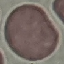
Summary:
  - Malaria status: uninfected
  - Stain: Giemsa
  - Image type: cell patch, automatically extracted from a larger field of view and resized to 64 × 64 pixels
  - Capture: smartphone through the microscope eyepiece
  - Preparation: thin smear